Give the extent of all Plasmodium falciparum-infected red blood cells.
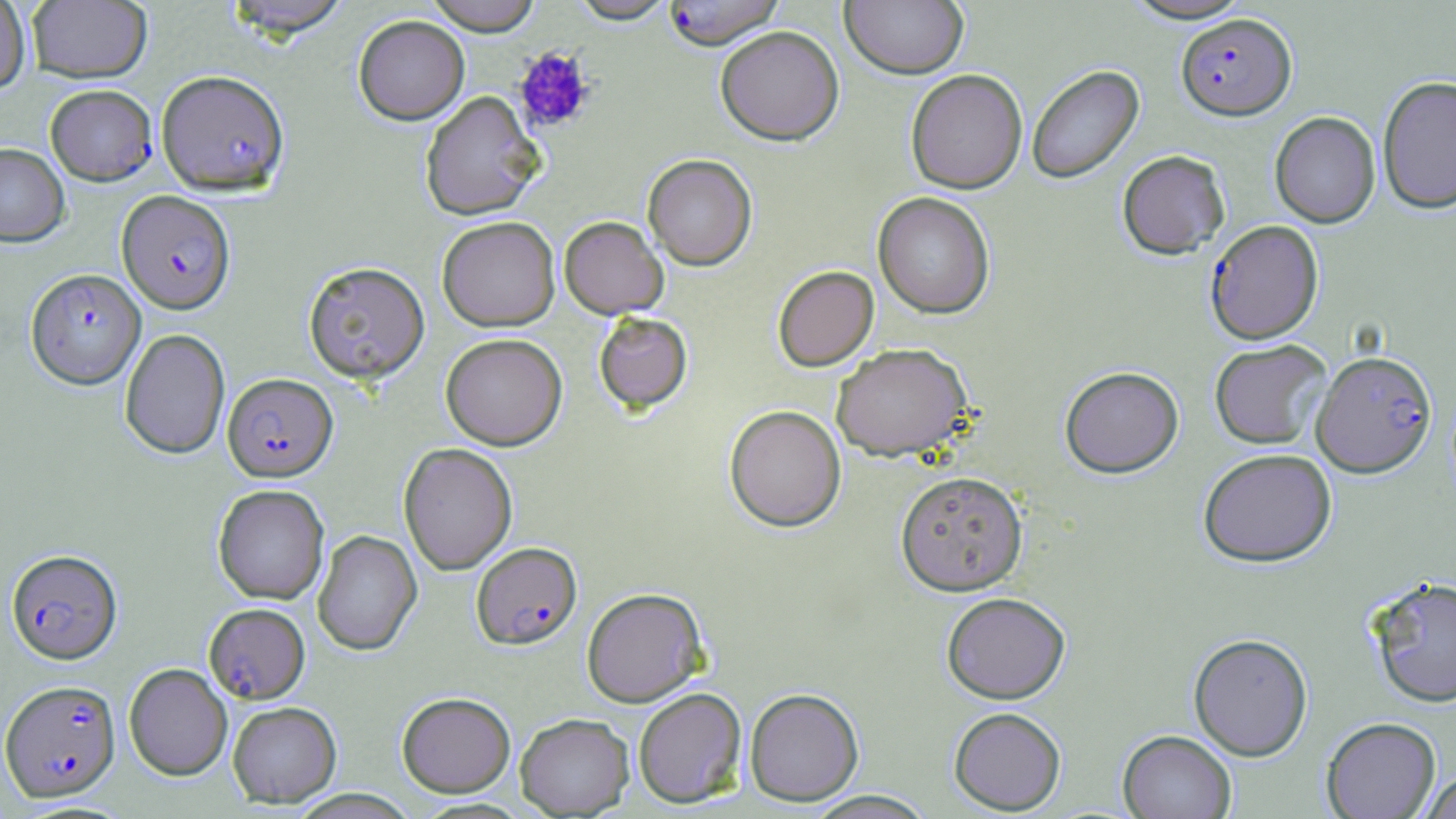

Approximate bounding boxes as [x1, y1, x2, y2] in pixels.
Plasmodium falciparum-infected red blood cells (subset): [1176, 14, 1296, 122], [45, 84, 157, 185], [116, 190, 236, 314], [1205, 221, 1324, 344], [24, 267, 144, 387], [1312, 350, 1437, 478], [223, 372, 337, 482], [471, 542, 582, 650], [6, 548, 122, 664], [204, 603, 310, 703], [1, 679, 121, 802].

Summary:
  - Uninfected red blood cell locations (subset): [0, 0, 31, 95], [27, 0, 152, 83], [222, 0, 353, 38], [423, 0, 543, 35], [568, 0, 678, 24], [1120, 0, 1255, 24], [840, 1, 968, 79], [353, 15, 470, 125], [714, 25, 844, 146], [1027, 64, 1145, 185], [156, 69, 290, 195], [905, 69, 1028, 194], [1377, 74, 1456, 215], [420, 91, 545, 220], [1270, 112, 1380, 228], [0, 142, 70, 247], [1117, 150, 1230, 260], [643, 154, 757, 271], [873, 192, 995, 319], [437, 216, 560, 331], [559, 216, 669, 318], [303, 261, 430, 383], [773, 266, 878, 371], [594, 313, 692, 413], [119, 328, 230, 459], [441, 333, 567, 450], [1209, 340, 1331, 450], [831, 343, 973, 461], [1060, 367, 1184, 479], [724, 405, 846, 532], [399, 443, 518, 575], [1198, 448, 1336, 568], [895, 471, 1028, 596], [212, 484, 329, 604], [313, 530, 422, 656], [1367, 575, 1456, 709], [582, 587, 708, 707], [941, 593, 1071, 704], [1188, 634, 1313, 762], [124, 663, 233, 781], [633, 687, 747, 808], [744, 688, 864, 806], [397, 691, 515, 797], [227, 701, 342, 807], [949, 707, 1066, 815], [515, 713, 634, 817], [1321, 718, 1441, 819], [1118, 730, 1236, 819], [1420, 771, 1456, 819], [804, 790, 938, 818]
  - Platelet locations: [512, 46, 596, 134]
  - Slide-level diagnosis: Plasmodium falciparum
  - Image size: 1456×819 pixels
  - Preparation: thin blood film
  - Modality: optical microscopy
  - Stain: May-Grünwald-Giemsa
  - Magnification: 1000x
  - Field of view: single